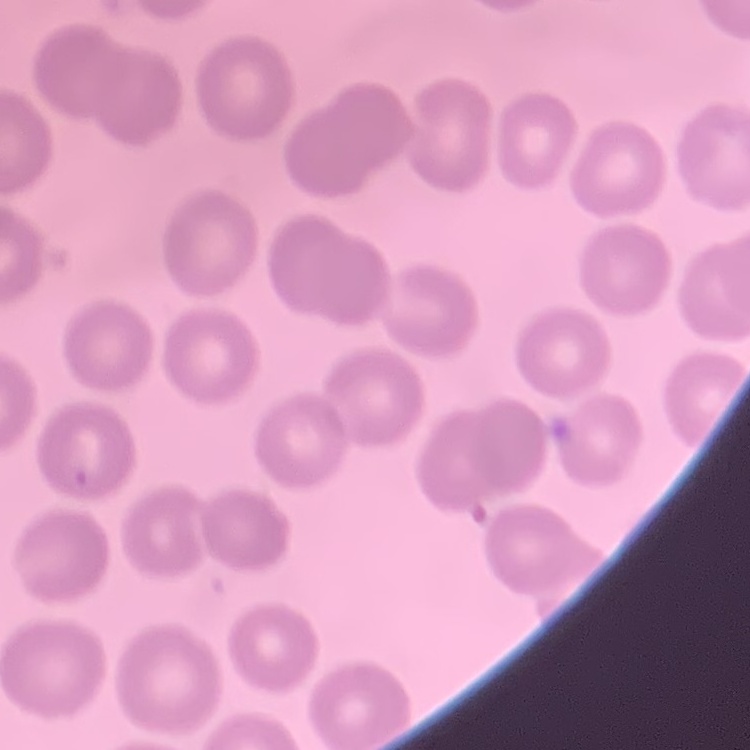
erythrocyte morphology = no rouleaux formation
image type = one tile cut from a larger photomicrograph
preparation = thin blood film
stain = Field's or Giemsa